Comment on the morphology of the erythrocytes.
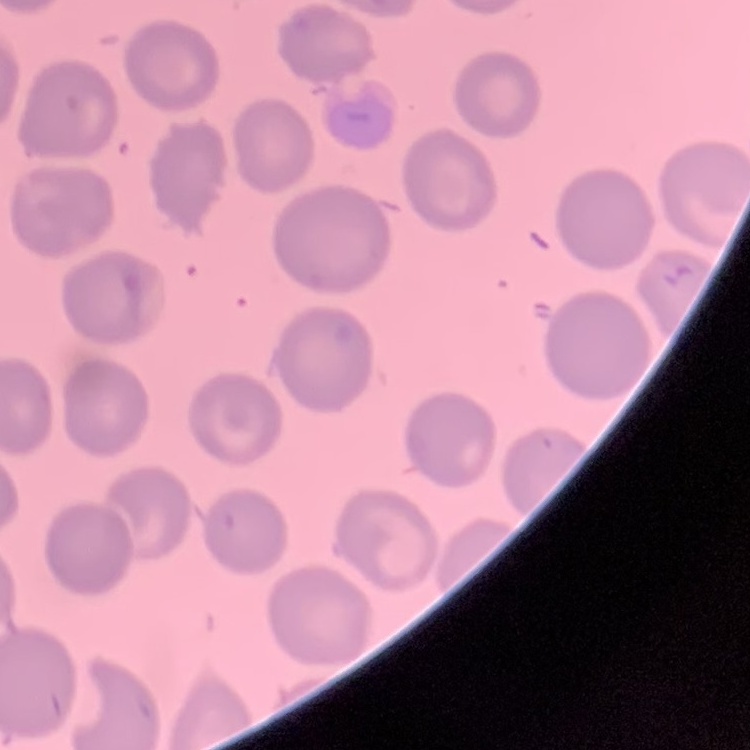
No rouleaux formation.

preparation = thin blood smear
image type = one tile cut from a larger photomicrograph
stain = Field's or Giemsa